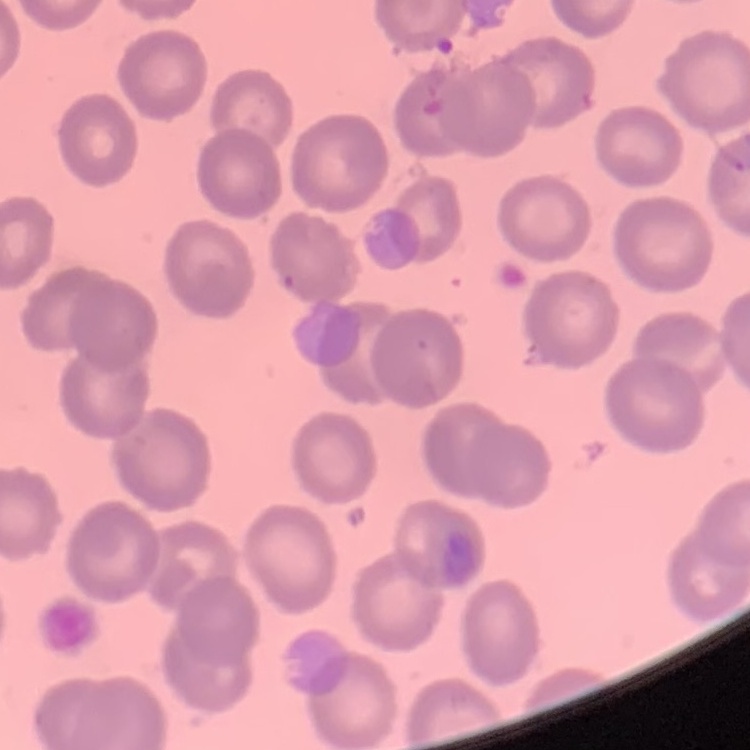
{
  "erythrocyte_morphology": "no rouleaux formation",
  "stain": "Field's or Giemsa",
  "preparation": "thin blood film",
  "image_type": "square crop of a larger photomicrograph"
}